Locate every P. falciparum parasite and give its life-cycle stage, and locate every leukocyte and any debris.
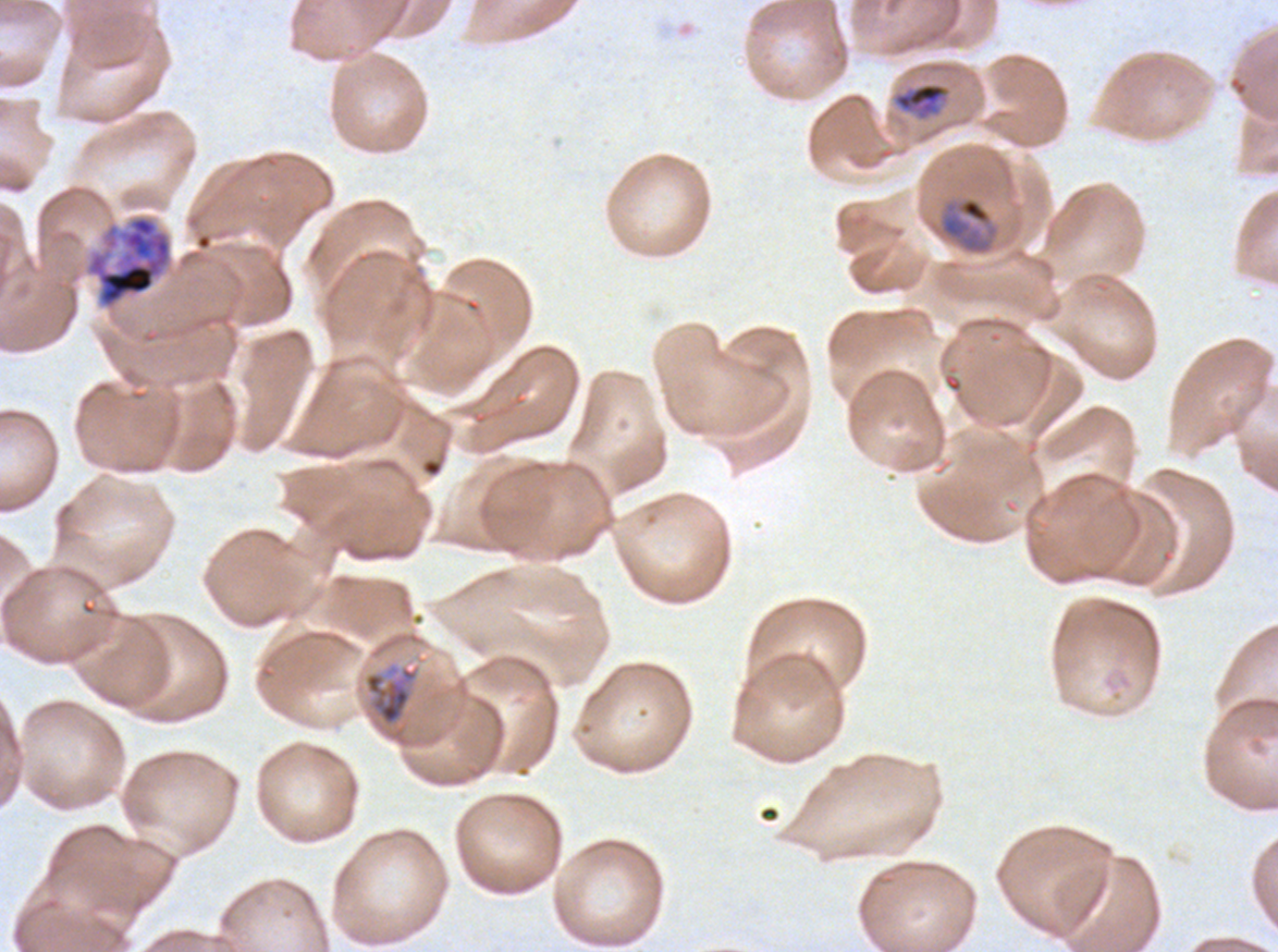

Approximate bounding boxes as [x1, y1, x2, y2] in pixels.
Mid trophozoites: [894, 82, 947, 115], [938, 196, 1000, 255], [363, 664, 420, 727].
Early schizonts: [83, 214, 174, 311].
No rings, late-ring/early-trophozoite forms, late trophozoites, late schizonts, segmenters, gametocytes, leukocytes, or debris observed.

specimen: P. falciparum cultured ex vivo for 24 to 48 hours, from a patient in The Gambia
life_cycle_stages_observed: mid trophozoite, early schizont
image_size: 1278×952 pixels
field_of_view: one sub-image of a larger composite
stain: Giemsa
preparation: thin blood smear